Comment on the morphology of the erythrocytes.
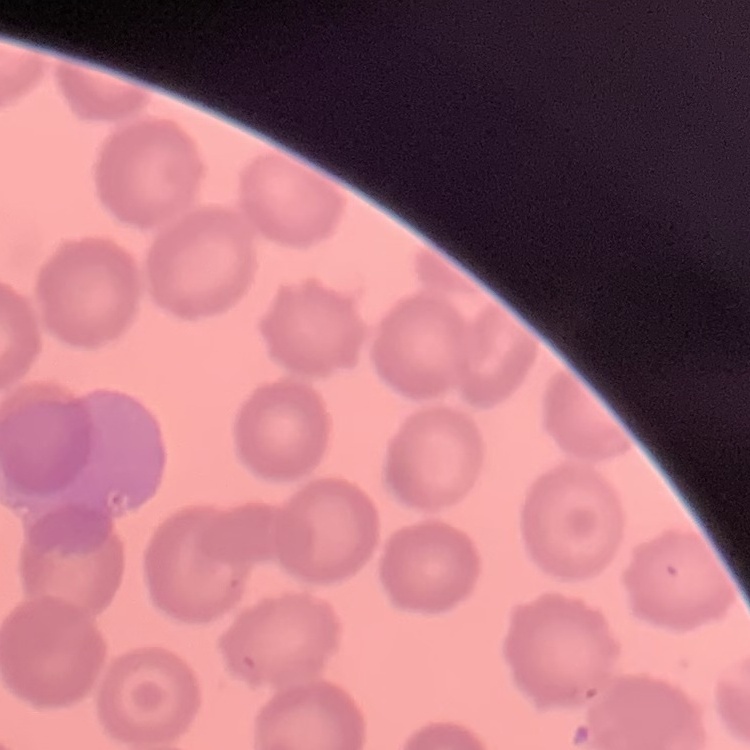
They show no rouleaux formation.

Summary:
  - Image type: square crop of a larger photomicrograph
  - Stain: Field's or Giemsa
  - Preparation: thin blood smear